Give the position of every Plasmodium parasite.
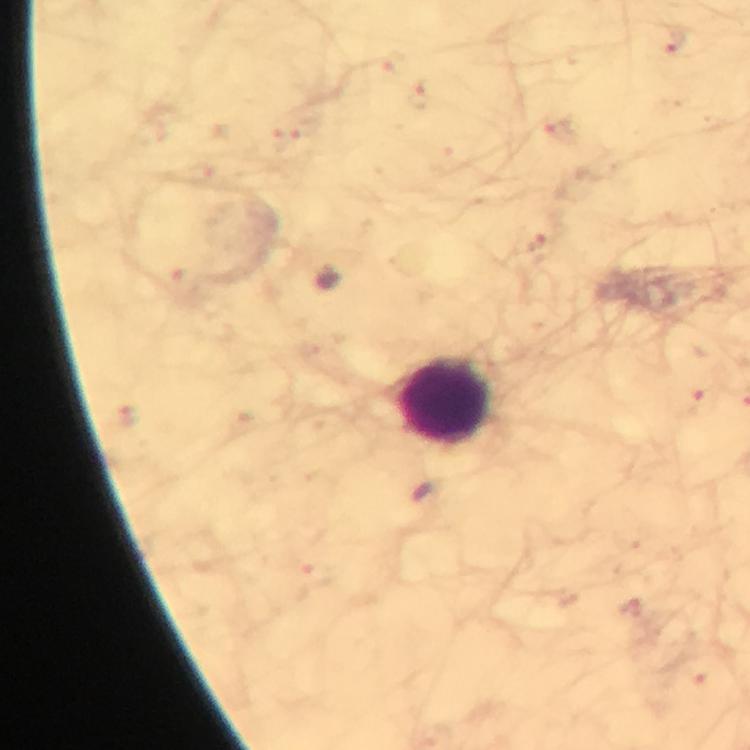

No Plasmodium parasites seen.

{
  "preparation": "thick blood film",
  "magnification": "100x",
  "image_size": "750×750 pixels",
  "immersion_oil": "applied",
  "leukocyte_locations": "approximate centers as {x, y} in pixels: {446, 401}",
  "context": "from a diagnostic examination for malaria",
  "stain": "Giemsa",
  "capture": "smartphone photograph through a microscope",
  "cropped_from": "a single field of view"
}